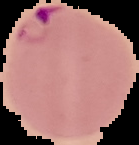

result: malaria parasites detected
image_size: 139×145 pixels
image_type: segmented cell region on a black background
preparation: thin blood film